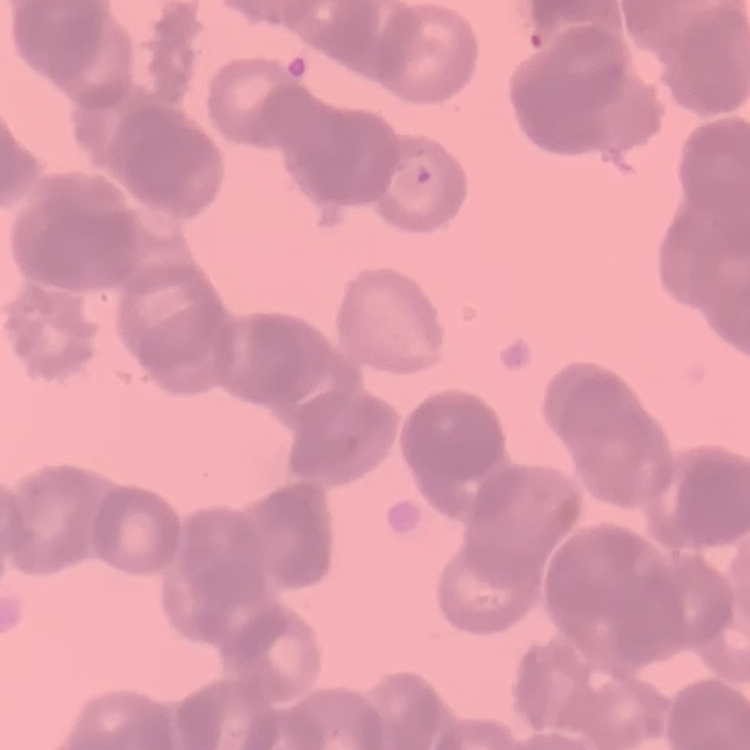 The erythrocytes exhibit rouleaux formation. Stained with either Field's or Giemsa. Square crop of a larger photomicrograph. Thin blood film.